Assess for malaria.
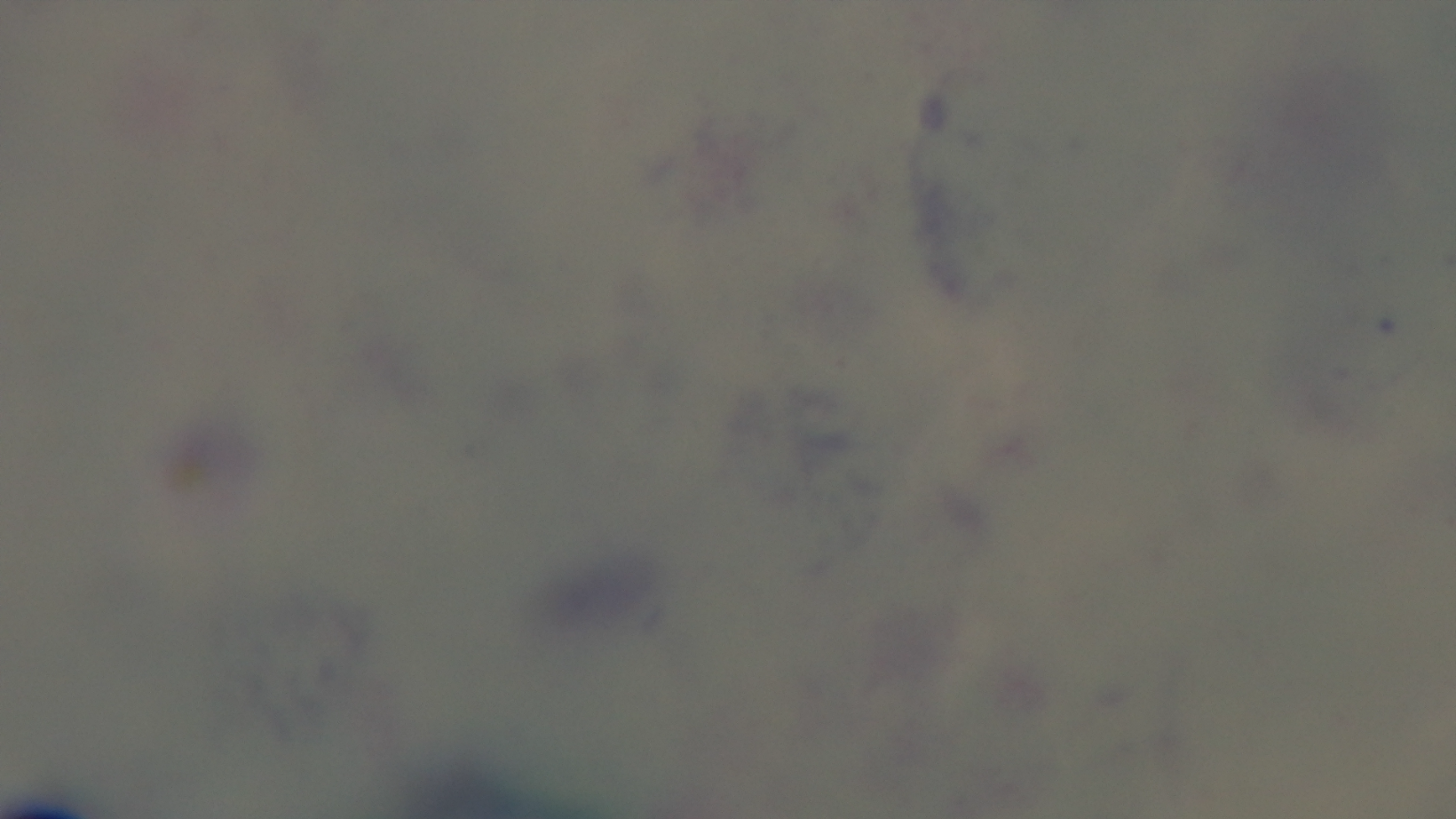
Uninfected.

modality: light microscopy
capture: mounted 4K digital camera
objective: 100x oil immersion
stain: Giemsa
field_of_view: single
preparation: thick